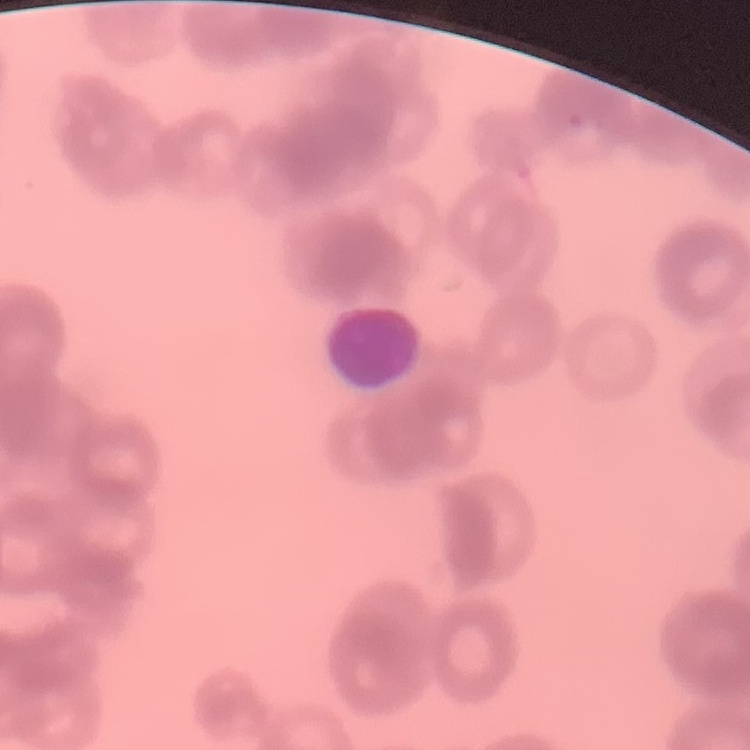

red_blood_cell_morphology: rouleaux formation
image_type: one tile cut from a larger photomicrograph
stain: Field's or Giemsa
preparation: thin peripheral smear